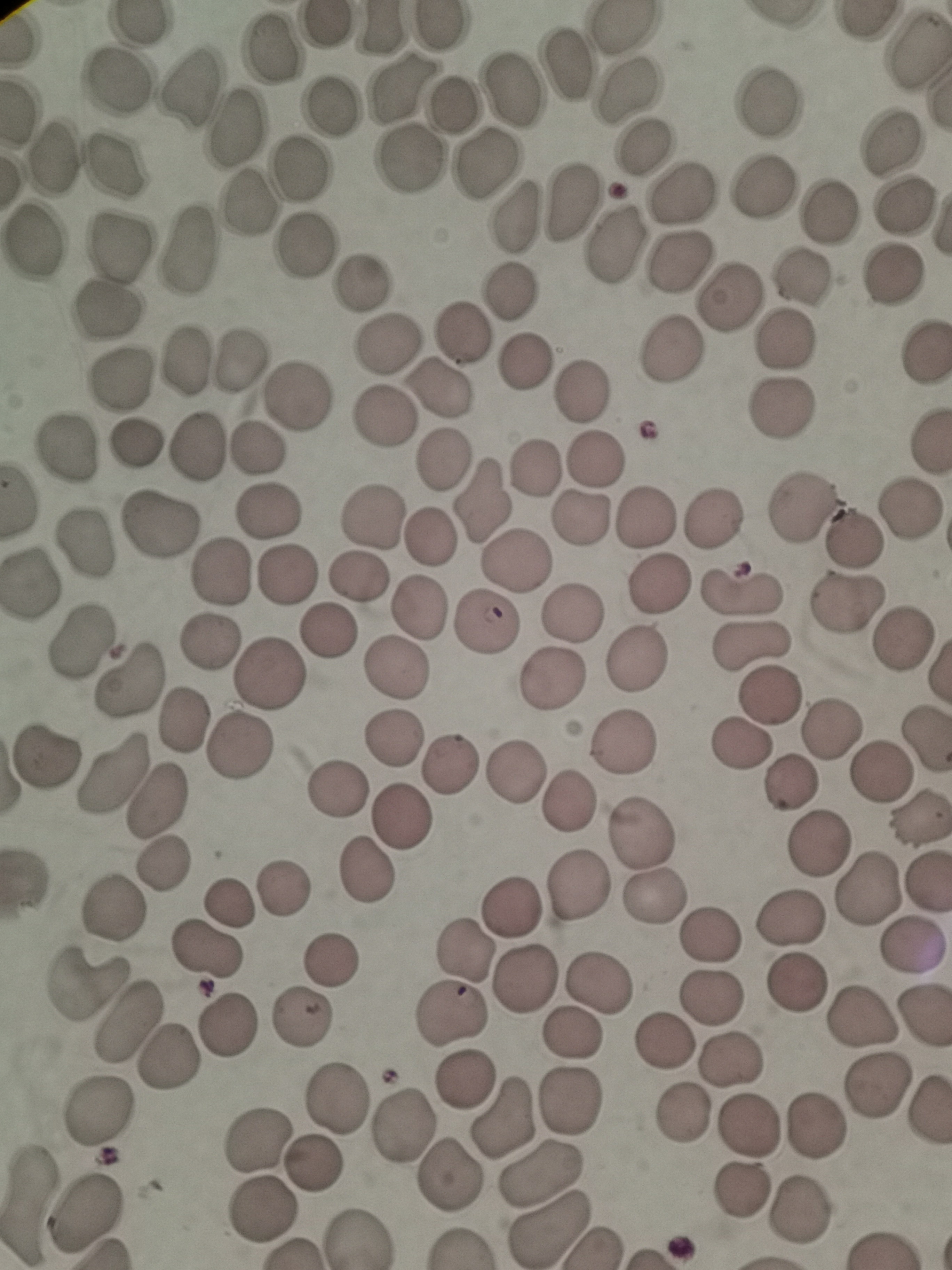
Approximate centers as {x, y} in pixels. Cell locations: {271, 49}, {916, 49}, {569, 65}, {115, 79}, {517, 87}, {404, 88}, {184, 89}, {626, 89}, {453, 104}, {768, 104}, {335, 105}, {235, 129}, {895, 142}, {642, 148}, {54, 156}, {409, 159}, {485, 161}, {117, 165}, {302, 167}, {761, 187}, {683, 196}, {571, 199}, {249, 200}, {904, 204}, {830, 210}, {515, 215}, {34, 240}, {118, 245}, {307, 245}, {616, 247}, {181, 249}, {679, 263}, {888, 272}, {799, 277}, {360, 283}, {509, 291}, {729, 296}, {109, 310}, {462, 337}, {780, 342}, {388, 344}, {668, 351}, {925, 351}, {181, 358}, {239, 360}, {525, 360}, {119, 381}, {440, 389}, {579, 392}, {298, 394}, {785, 408}, {382, 416}, {135, 442}, {198, 446}, {257, 447}, {64, 448}, {443, 457}, {597, 460}, {534, 468}, {483, 498}, {800, 505}, {910, 506}, {269, 512}, {713, 517}, {644, 518}, {372, 519}, {577, 519}, {162, 527}, {427, 536}, {851, 538}, {87, 544}, {515, 558}, {285, 572}, {217, 576}, {359, 577}, {33, 582}, {663, 586}, {741, 590}, {846, 603}, {417, 605}, {569, 611}, {487, 625}, {329, 631}, {82, 642}, {904, 642}, {213, 643}, {750, 646}, {638, 657}, {394, 671}, {271, 673}, {554, 678}, {130, 680}, {771, 693}, {184, 721}, {831, 730}, {395, 739}, {625, 740}, {925, 740}, {739, 746}, {241, 748}, {46, 756}, {451, 766}, {515, 769}, {881, 769}, {112, 771}, {791, 782}, {340, 789}, {567, 801}, {155, 802}, {400, 816}, {917, 818}, {641, 833}, {815, 844}, {163, 866}, {364, 869}, {289, 883}, {579, 884}, {868, 887}, {654, 899}, {228, 905}, {510, 906}, {114, 907}, {787, 919}, {711, 933}, {911, 943}, {464, 948}, {206, 951}, {331, 957}, {524, 979}, {599, 981}, {795, 981}, {87, 984}, {712, 996}, {923, 1015}, {452, 1016}, {863, 1016}, {302, 1018}, {128, 1023}, {227, 1024}, {572, 1031}, {660, 1040}, {733, 1056}, {168, 1057}, {466, 1081}, {873, 1083}, {339, 1098}, {569, 1103}, {103, 1109}, {685, 1113}, {504, 1116}, {748, 1123}, {814, 1125}, {406, 1127}, {257, 1145}, {316, 1164}, {545, 1173}, {448, 1177}, {741, 1191}, {30, 1201}, {86, 1209}, {799, 1210}, {264, 1211}, {552, 1230}. Thin blood film. One field from this slide. Giemsa stain. Acquired by smartphone through the microscope eyepiece. Image is 952×1270 pixels.